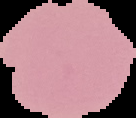
{
  "image_type": "segmented cell region on a black background",
  "image_size": "136×118 pixels",
  "preparation": "thin blood smear",
  "malaria_status": "uninfected"
}